Assess this cell for malaria.
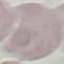
It is uninfected.

Summary:
  - Image type: automatically extracted cell patch, resized to 64 × 64 pixels
  - Preparation: thin smear
  - Capture: smartphone camera at the microscope eyepiece
  - Stain: Giemsa